Give the extent of all Plasmodium falciparum-infected red blood cells.
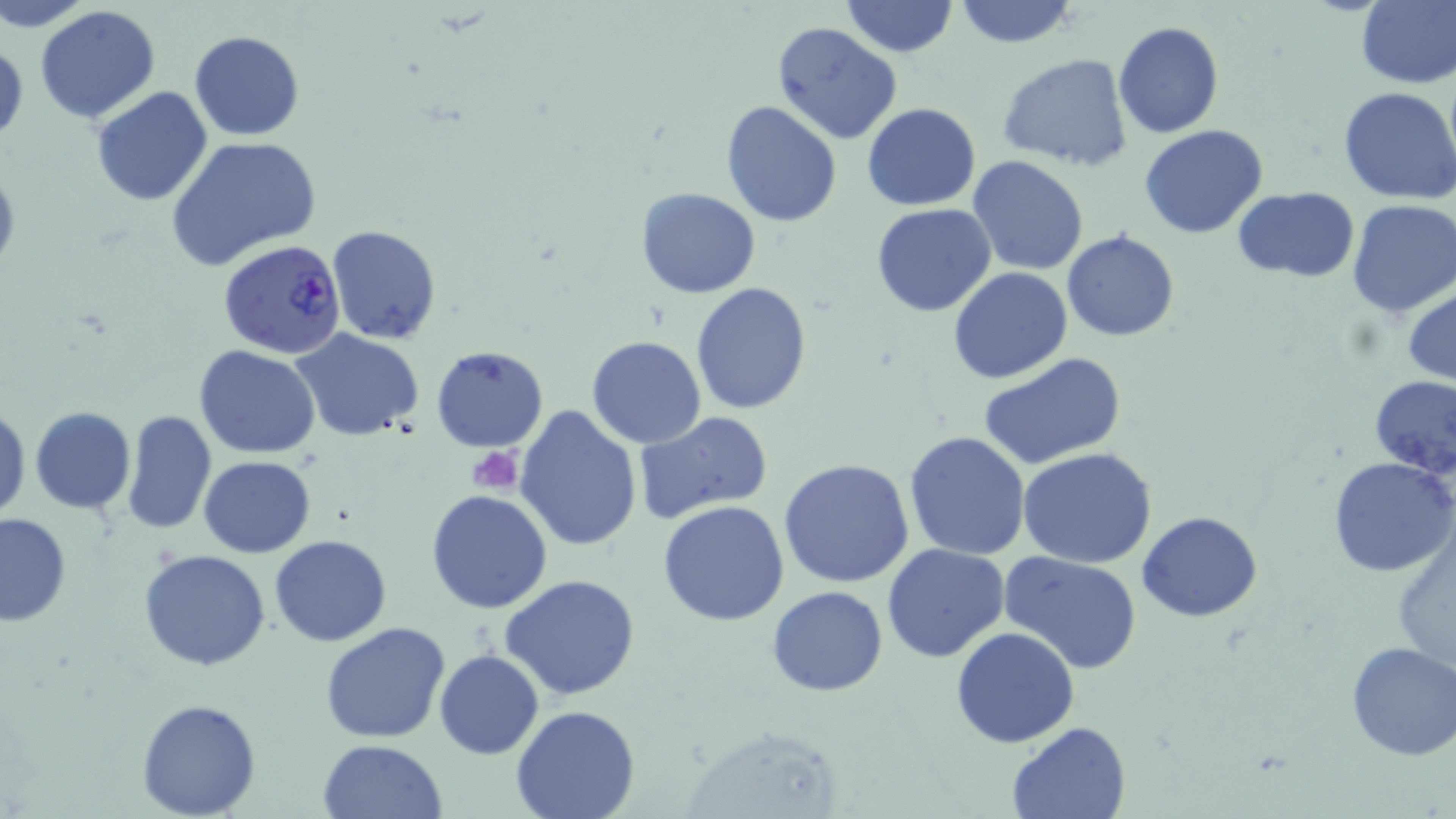

Approximate bounding boxes as (x1,y1)-(x2,y2) corner pairs in pixels.
Plasmodium falciparum-infected red blood cells: (217,237)-(348,359).

Summary:
  - Platelet locations: (467,447)-(523,495)
  - Uninfected red blood cell locations: (1,0)-(96,31), (953,0)-(1078,49), (841,1)-(958,58), (1354,2)-(1456,87), (34,6)-(161,125), (772,20)-(903,145), (1113,21)-(1224,138), (190,30)-(305,142), (1,37)-(26,150), (996,54)-(1135,171), (1338,86)-(1456,204), (92,87)-(213,206), (721,100)-(844,227), (863,103)-(980,211), (1140,125)-(1270,239), (167,136)-(320,268), (967,156)-(1088,275), (0,159)-(20,277), (1232,186)-(1359,282), (636,188)-(761,297), (1346,200)-(1456,318), (870,202)-(996,317), (325,224)-(443,345), (1063,231)-(1179,342), (949,266)-(1073,383), (690,283)-(813,415), (1404,286)-(1456,386), (292,328)-(424,441), (587,335)-(707,448), (431,345)-(549,453), (194,346)-(322,459), (555,352)-(685,492), (978,352)-(1128,469), (1370,377)-(1456,480), (513,403)-(641,550), (0,405)-(28,522), (29,408)-(137,514), (121,408)-(217,536), (633,410)-(775,524), (904,430)-(1033,561), (1019,450)-(1158,568), (199,455)-(317,557), (1329,456)-(1456,577), (777,459)-(917,589), (426,489)-(554,613), (658,500)-(790,626), (1137,512)-(1263,622), (0,513)-(72,627), (268,534)-(392,648), (881,544)-(1010,663), (139,548)-(271,671), (1001,551)-(1143,673), (500,573)-(639,700), (767,586)-(889,696), (320,621)-(450,744), (951,628)-(1080,748), (1345,641)-(1456,760), (435,649)-(544,759), (136,699)-(260,818), (510,703)-(641,819), (1007,721)-(1131,818), (319,740)-(447,819)
  - Slide-level diagnosis: Plasmodium falciparum
  - Image size: 1456×819 pixels
  - Magnification: 1000x
  - Field of view: one of a larger specimen
  - Stain: May-Grünwald-Giemsa
  - Modality: optical microscopy
  - Preparation: thin blood smear